Outline each blood parasite and name the species.
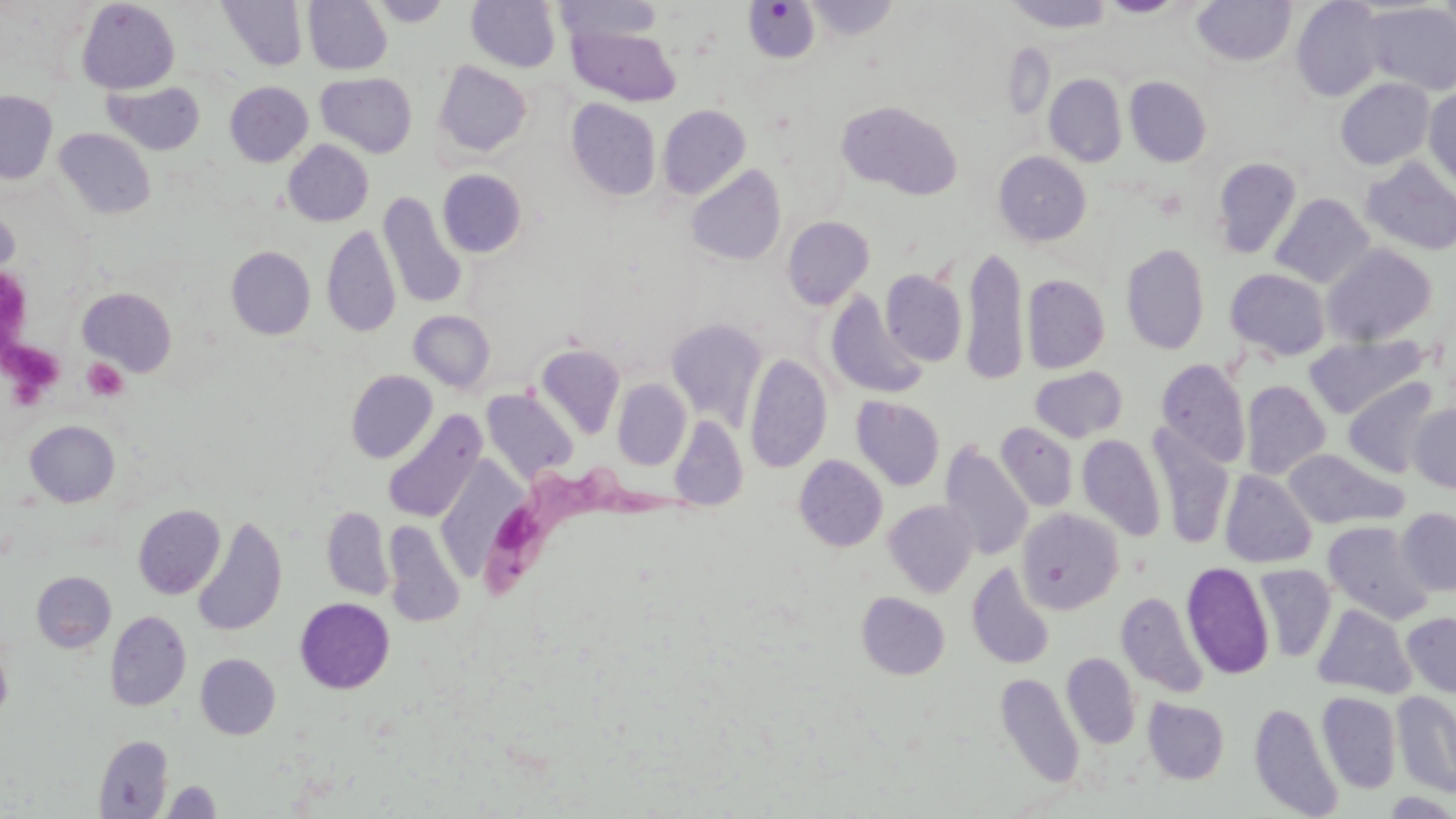
Approximate bounding boxes as (x1,y1)-(x2,y2) corner pairs in pixels.
Trypanosoma brucei: (469,451)-(694,605).
No Plasmodium falciparum, Plasmodium ovale, Plasmodium malariae, Plasmodium vivax, or Babesia divergens observed.

Platelet locations: (1,269)-(36,348), (3,336)-(62,400), (81,358)-(128,402). Uninfected red blood cell locations: (218,0)-(308,72), (303,0)-(392,74), (371,0)-(451,27), (466,0)-(561,73), (1005,0)-(1113,32), (1100,0)-(1185,18), (1192,0)-(1296,66), (1436,0)-(1456,42), (77,1)-(179,93), (555,1)-(663,45), (804,1)-(899,41), (1290,1)-(1384,101), (745,2)-(819,63), (1362,2)-(1456,96), (569,25)-(681,106), (433,61)-(532,158), (316,72)-(417,157), (1045,74)-(1127,167), (1125,76)-(1212,167), (1336,78)-(1434,170), (103,81)-(205,156), (225,81)-(313,167), (1424,87)-(1456,192), (0,91)-(58,184), (565,98)-(661,201), (837,100)-(962,199), (657,105)-(750,199), (54,128)-(156,220), (283,140)-(374,226), (994,151)-(1091,246), (1361,157)-(1456,255), (1211,158)-(1302,260), (686,165)-(786,266), (438,170)-(527,258), (378,191)-(468,308), (1270,193)-(1374,288), (782,216)-(875,310), (322,224)-(401,337), (1121,243)-(1209,354), (1321,243)-(1437,346), (962,244)-(1029,385), (226,246)-(315,339), (1224,268)-(1331,361), (881,269)-(967,366), (1022,274)-(1110,373), (77,288)-(177,376), (825,290)-(927,400), (409,310)-(495,392), (666,318)-(768,430), (1305,335)-(1427,418), (535,344)-(625,440), (745,354)-(831,473), (1156,359)-(1250,468), (1030,366)-(1128,442), (346,370)-(437,463), (1343,377)-(1440,478), (613,379)-(690,470), (1241,380)-(1331,480), (481,389)-(578,485), (851,396)-(945,491), (1409,403)-(1456,493), (383,410)-(486,523), (669,415)-(748,511), (25,420)-(120,507), (995,423)-(1078,512), (1149,426)-(1236,548), (1077,433)-(1166,541), (939,441)-(1033,561), (1282,448)-(1408,530), (794,455)-(887,551), (1220,469)-(1317,568), (884,499)-(978,597), (133,505)-(225,599), (321,506)-(394,600), (1017,508)-(1124,613), (1396,508)-(1456,596), (192,517)-(287,636), (1323,521)-(1434,625), (384,523)-(465,626), (967,562)-(1055,670), (1181,562)-(1275,679), (1254,564)-(1336,662), (32,571)-(116,652), (1116,591)-(1209,698), (856,592)-(950,679), (295,597)-(394,693), (1313,604)-(1416,698), (105,610)-(191,711), (1401,611)-(1456,698), (0,634)-(13,724), (1062,652)-(1140,748), (195,654)-(280,739), (997,676)-(1085,789), (1317,691)-(1401,793), (1392,691)-(1456,797), (1143,697)-(1230,784), (1248,702)-(1343,817), (94,735)-(174,818), (162,780)-(221,817). Slide-level diagnosis: Trypanosoma brucei. Captured at 1000x magnification. May-Grünwald-Giemsa-stained preparation. Thin blood film. Image is 1456×819 pixels. Optical microscopy. Single field of view.